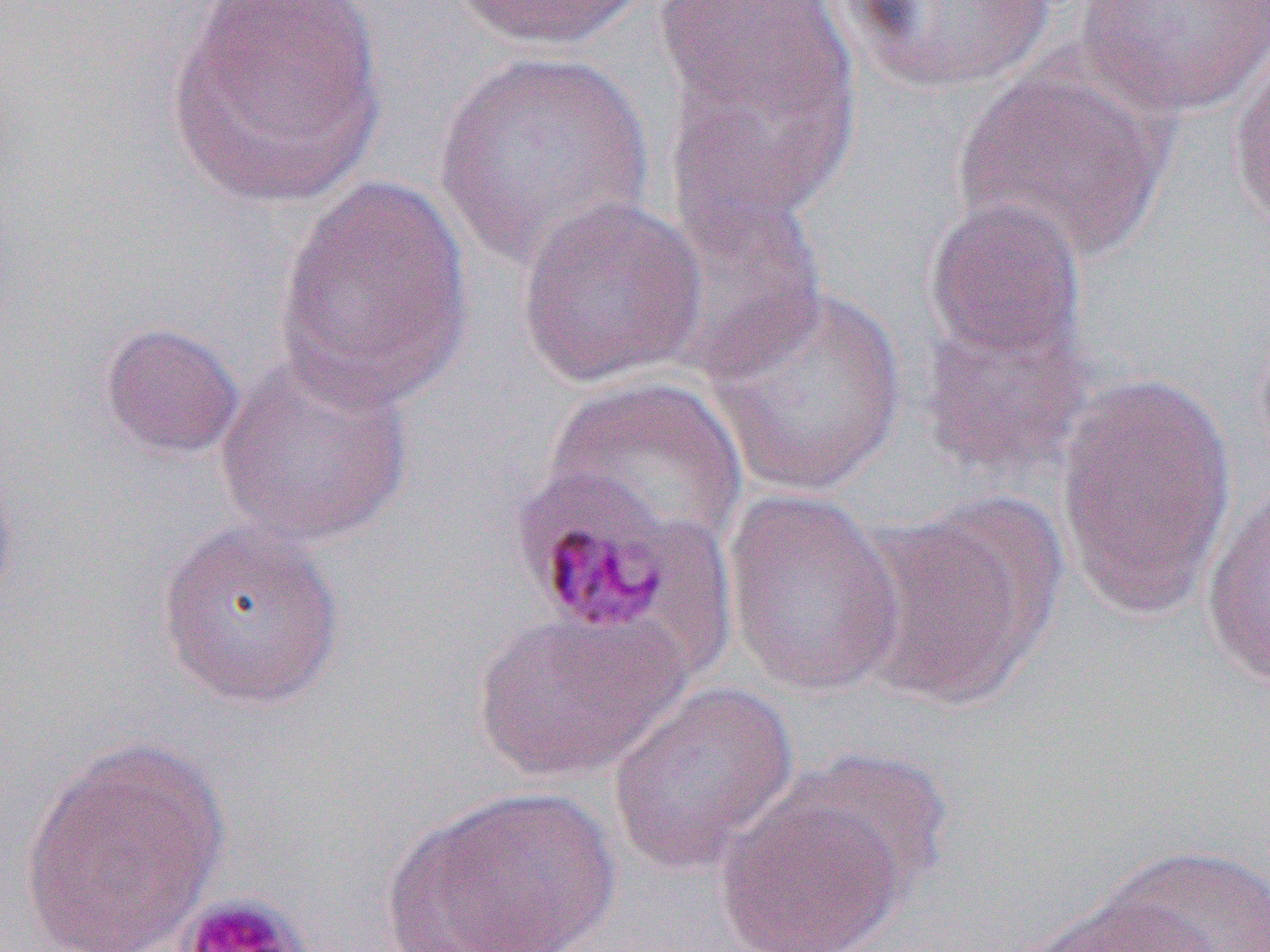
slide-level diagnosis = Plasmodium malariae
field of view = one of a larger specimen
platelet locations = approximate bounding boxes as [x1, y1, x2, y2] in pixels: [177, 893, 312, 952]
uninfected red blood cell locations = approximate bounding boxes as [x1, y1, x2, y2] in pixels: [166, 0, 387, 208], [453, 0, 645, 53], [840, 0, 1058, 94], [1075, 0, 1268, 119], [653, 1, 852, 127], [660, 35, 857, 246], [1228, 43, 1270, 230], [434, 49, 655, 272], [949, 66, 1174, 263], [273, 175, 473, 409], [661, 190, 828, 377], [514, 194, 708, 389], [922, 196, 1088, 365], [701, 283, 909, 498], [917, 312, 1094, 483], [99, 321, 246, 459], [214, 352, 415, 549], [1054, 371, 1240, 620], [540, 376, 749, 557], [0, 449, 20, 617], [1201, 484, 1270, 694], [722, 489, 907, 699], [854, 497, 1062, 710], [155, 519, 346, 709], [471, 609, 688, 784], [607, 679, 800, 877], [18, 738, 229, 950], [713, 783, 911, 952], [394, 784, 622, 952], [1089, 845, 1270, 951], [1023, 892, 1217, 952]
modality = light microscopy
Plasmodium malariae-infected red blood cell locations = approximate bounding boxes as [x1, y1, x2, y2] in pixels: [507, 467, 698, 641]
image size = 1270×952 pixels
preparation = thin blood smear
magnification = 1000x